Assess this cell for malaria.
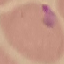
Parasitized.

Thin blood smear. Automatically extracted cell patch, resized to 64 × 64 pixels. Acquired by smartphone through the microscope eyepiece. Giemsa-stained preparation.